Report the malaria status of this cell.
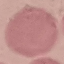
It is uninfected.

image type = cell patch, automatically extracted from a larger field of view and resized to 64 × 64 pixels
preparation = thin blood film
stain = Giemsa
capture = smartphone camera at the microscope eyepiece